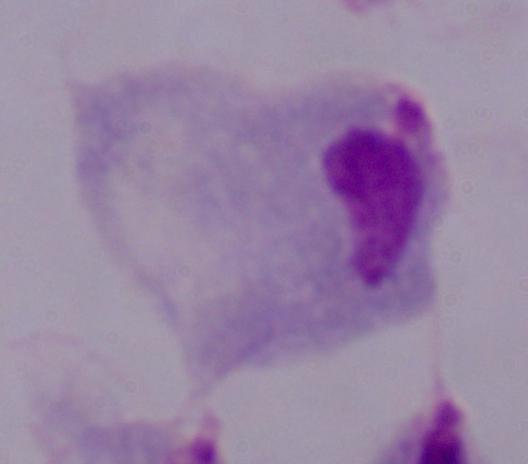
{
  "identification": "trichomonad",
  "modality": "photomicrograph",
  "magnification": "1000x"
}